Outline every leukocyte.
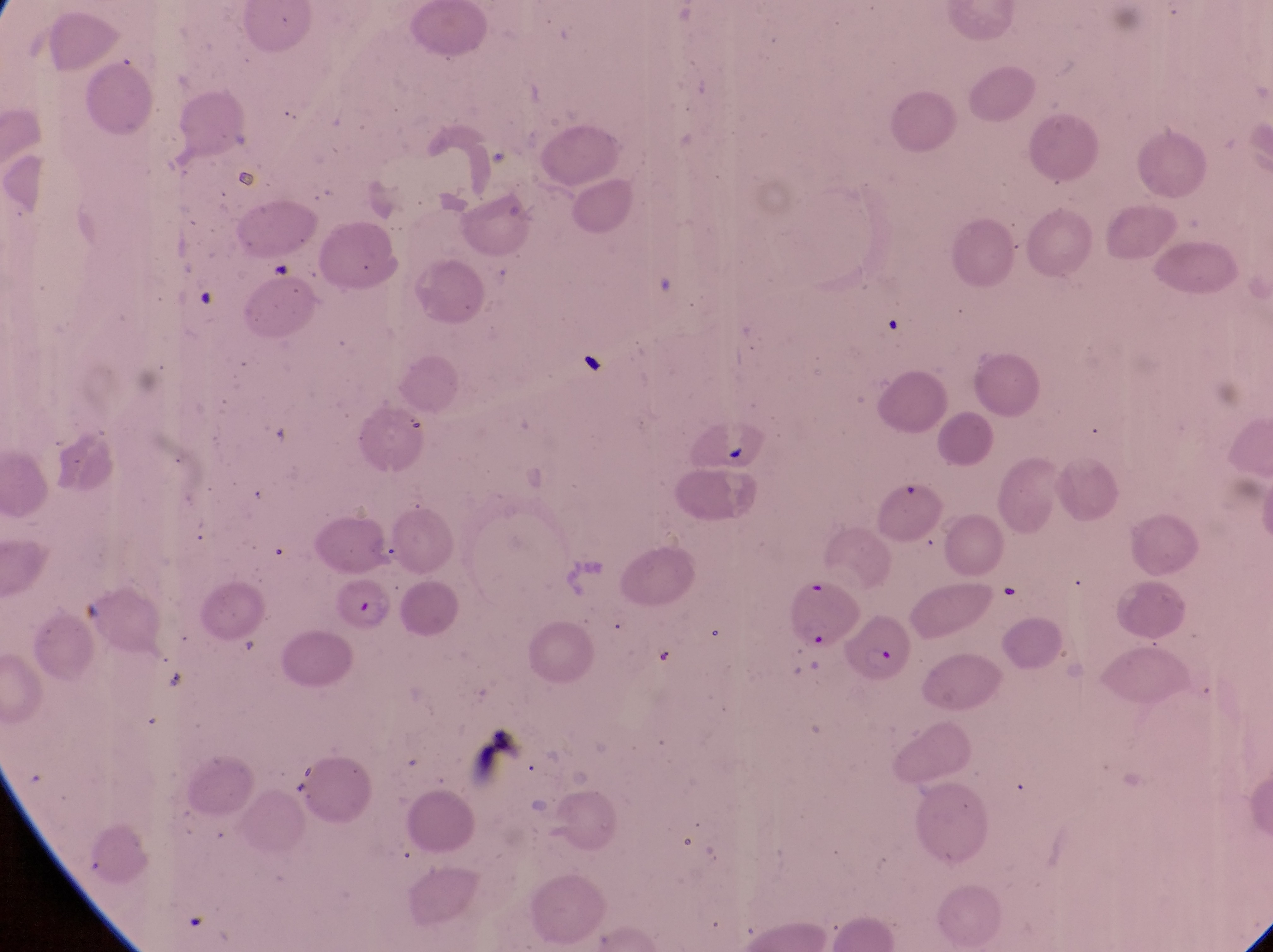
No leukocytes observed.

capture = smartphone photograph through the eyepiece of an Olympus CX-23 microscope
parasitised red blood cell locations = approximate bounding boxes as (left, top, right, bottom) in pixels: (330, 574, 402, 641), (789, 577, 854, 647), (852, 614, 910, 686)
magnification = 1000x
country = Uganda
preparation = thin blood smear
image size = 1273×952 pixels
field of view = single